State which parasite is depicted.
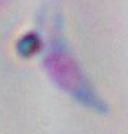
Toxoplasma gondii.

magnification = 1000x
modality = photomicrograph